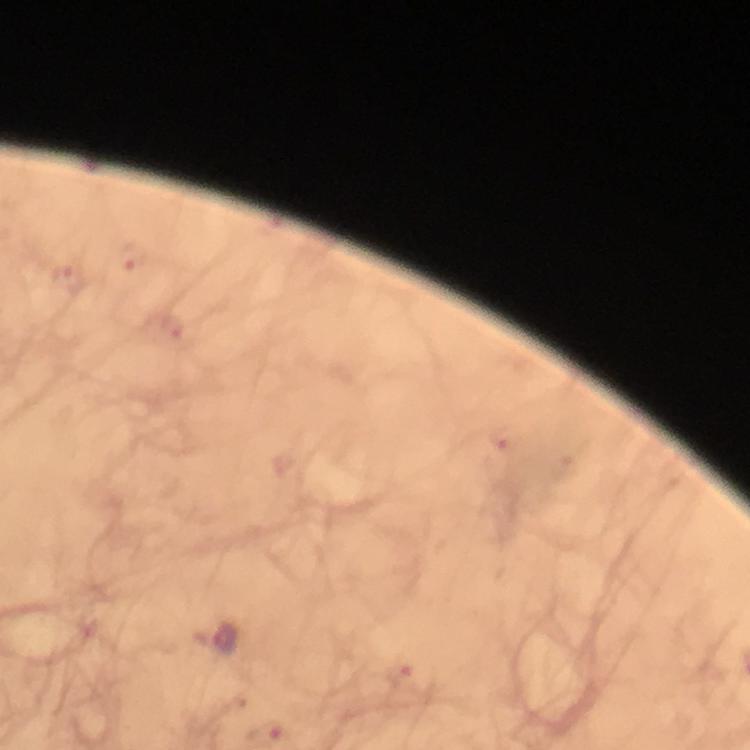 Approximate centers as {x, y} in pixels. Malaria parasite locations: {132, 256}, {67, 275}, {169, 328}, {504, 437}, {226, 639}, {401, 674}, {266, 733}. A crop from one field of view. At 100x magnification. From a malaria diagnostic workup. Thick smear. Image is 750×750 pixels. Photographed through the microscope with a smartphone camera. Immersion oil applied. Giemsa stain.